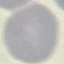

malaria_status: uninfected
image_type: cell patch, automatically extracted from a larger field of view and resized to 64 × 64 pixels
capture: smartphone through the microscope eyepiece
preparation: thin smear
stain: Giemsa